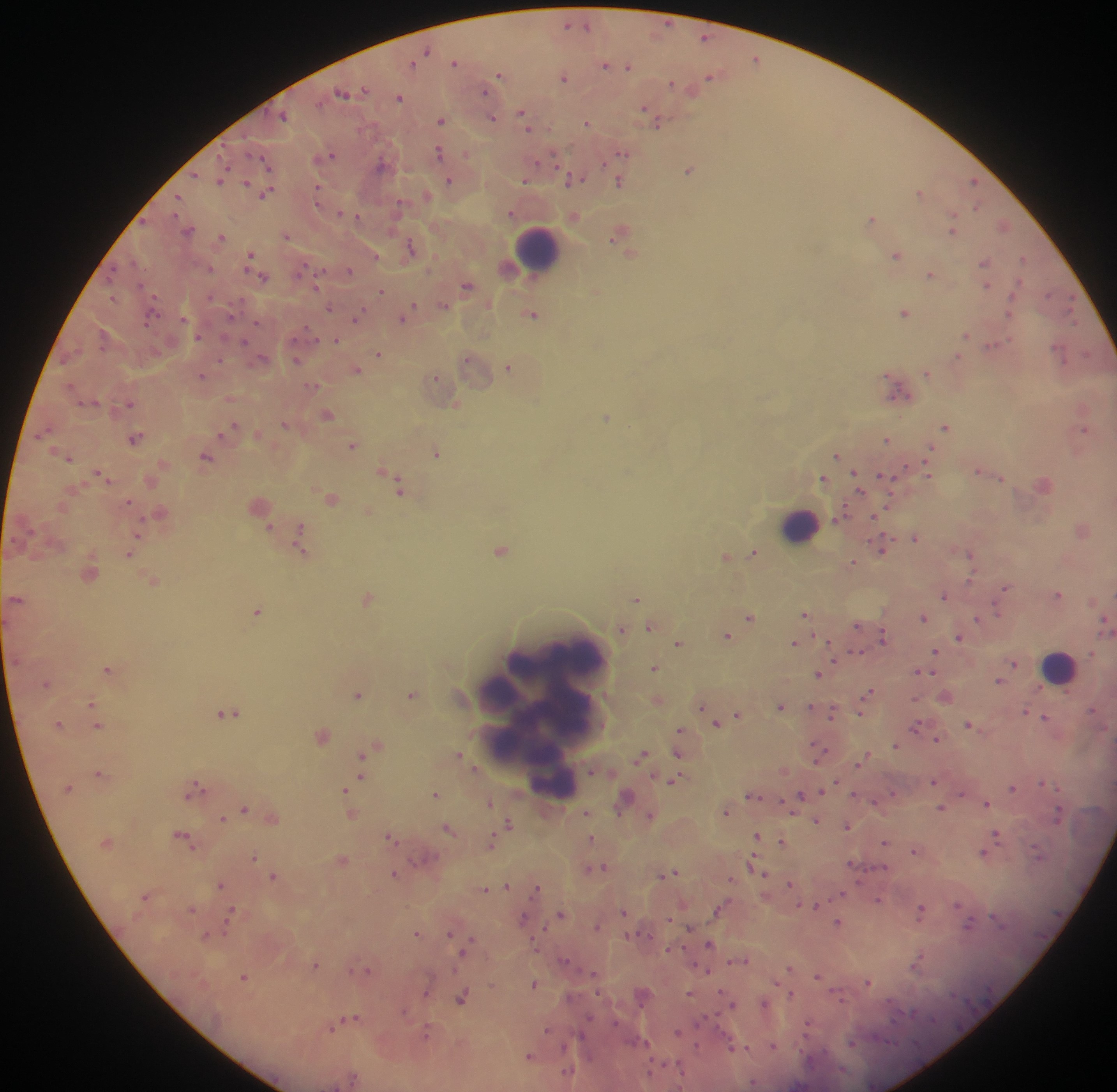

Approximate centers as x y in pixels. Malaria parasite locations: 567 24; 587 25; 705 37; 427 50; 755 58; 455 61; 412 64; 605 64; 629 65; 500 74; 565 77; 710 77; 671 84; 365 90; 484 91; 693 91; 342 93; 399 97; 644 109; 522 114; 284 116; 493 118; 653 118; 441 120; 586 123; 658 123; 527 125; 439 152; 466 154; 622 154; 332 155; 263 160; 539 162; 381 164; 225 167; 690 170; 195 175; 221 179; 571 180; 449 181; 526 181; 246 182; 973 182; 620 183; 318 189; 920 192; 266 193; 427 195; 178 197; 318 198; 399 204; 977 207; 340 212; 511 212; 175 213; 356 216; 872 218; 1003 225; 952 226; 189 230; 286 236; 616 236; 222 237; 411 247; 630 254; 250 255; 895 255; 376 256; 1023 258; 135 262; 984 262; 302 268; 210 269; 349 270; 931 274; 264 278; 316 285; 466 285; 986 286; 382 291; 595 291; 1049 294; 210 297; 112 298; 443 305; 413 306; 1070 306; 329 308; 905 312; 532 314; 230 315; 357 317; 1074 317; 150 318; 183 318; 403 319; 257 323; 308 330; 965 335; 199 337; 336 340; 245 342; 994 345; 1059 352; 1086 353; 378 354; 958 356; 262 358; 221 361; 297 361; 509 368; 356 370; 927 373; 202 376; 435 377; 312 386; 71 387; 897 390; 130 403; 456 404; 328 414; 607 417; 285 424; 946 427; 231 429; 47 430; 1083 430; 135 439; 886 439; 353 446; 930 450; 437 453; 836 455; 206 457; 69 458; 385 470; 978 471; 102 474; 928 474; 856 477; 885 477; 823 478; 1000 478; 399 488; 858 489; 331 499; 128 502; 842 514; 874 516; 270 527; 300 529; 138 537; 915 537; 299 539; 883 546; 301 549; 500 550; 753 553; 130 554; 970 554; 725 557; 852 563; 970 579; 153 582; 1005 589; 1059 594; 944 596; 368 599; 635 599; 257 611; 998 612; 804 614; 750 617; 923 617; 977 618; 1104 621; 857 625; 650 628; 621 630; 727 636; 882 638; 958 638; 678 644; 794 644; 855 652; 935 652; 1092 654; 834 659; 1014 664; 655 668; 107 669; 918 672; 817 674; 999 681; 47 684; 867 692; 358 695; 411 695; 91 704; 701 707; 781 707; 810 707; 1093 709; 860 712; 1025 712; 228 713; 832 714; 738 715; 1045 717; 59 724; 718 724; 968 724; 98 725; 915 726; 680 731; 322 736; 937 740; 895 745; 377 746; 677 753; 818 754; 459 755; 641 755; 863 758; 363 760; 99 773; 361 774; 674 780; 934 782; 835 783; 1042 783; 196 788; 1012 788; 1059 788; 346 789; 893 793; 962 793; 435 795; 752 795; 854 795; 800 796; 625 798; 489 802; 987 803; 244 808; 941 808; 726 812; 586 813; 351 815; 1058 815; 650 816; 223 818; 816 821; 509 823; 847 826; 448 829; 756 835; 997 835; 390 837; 184 838; 591 840; 781 841; 885 843; 490 844; 914 852; 1038 852; 982 853; 254 858; 342 859; 423 859; 753 862; 851 864; 602 867; 395 873; 670 873; 765 874; 273 878; 731 879; 790 883; 221 886; 507 886; 484 889; 536 889; 841 894; 146 896; 878 900; 957 904; 816 906; 720 909; 191 911; 920 911; 624 912; 560 915; 230 916; 523 919; 670 919; 997 919; 838 923; 970 924; 597 926; 690 928; 417 933; 449 934; 205 936; 471 942; 709 944; 668 950; 464 951; 564 960; 918 960; 745 961; 315 965; 790 968; 705 970; 369 971; 594 973; 818 975; 243 977; 534 983; 868 983; 427 991; 690 994; 790 995; 461 999; 764 1004; 732 1006; 403 1012; 354 1018; 588 1019; 615 1023; 808 1024; 333 1026; 547 1030; 678 1032; 426 1033; 640 1041; 851 1044; 697 1046; 773 1046; 565 1047; 733 1047; 744 1048; 528 1055; 651 1069; 567 1072. Leukocyte locations: 538 247; 799 524; 1060 666; 496 696; 543 719; 555 781. Image is 1117×1092 pixels. Sample from Ghana. Thick blood film. One field of view. Photographed through a microscope with a mobile-phone camera.